Locate every Plasmodium ovale-infected red blood cell.
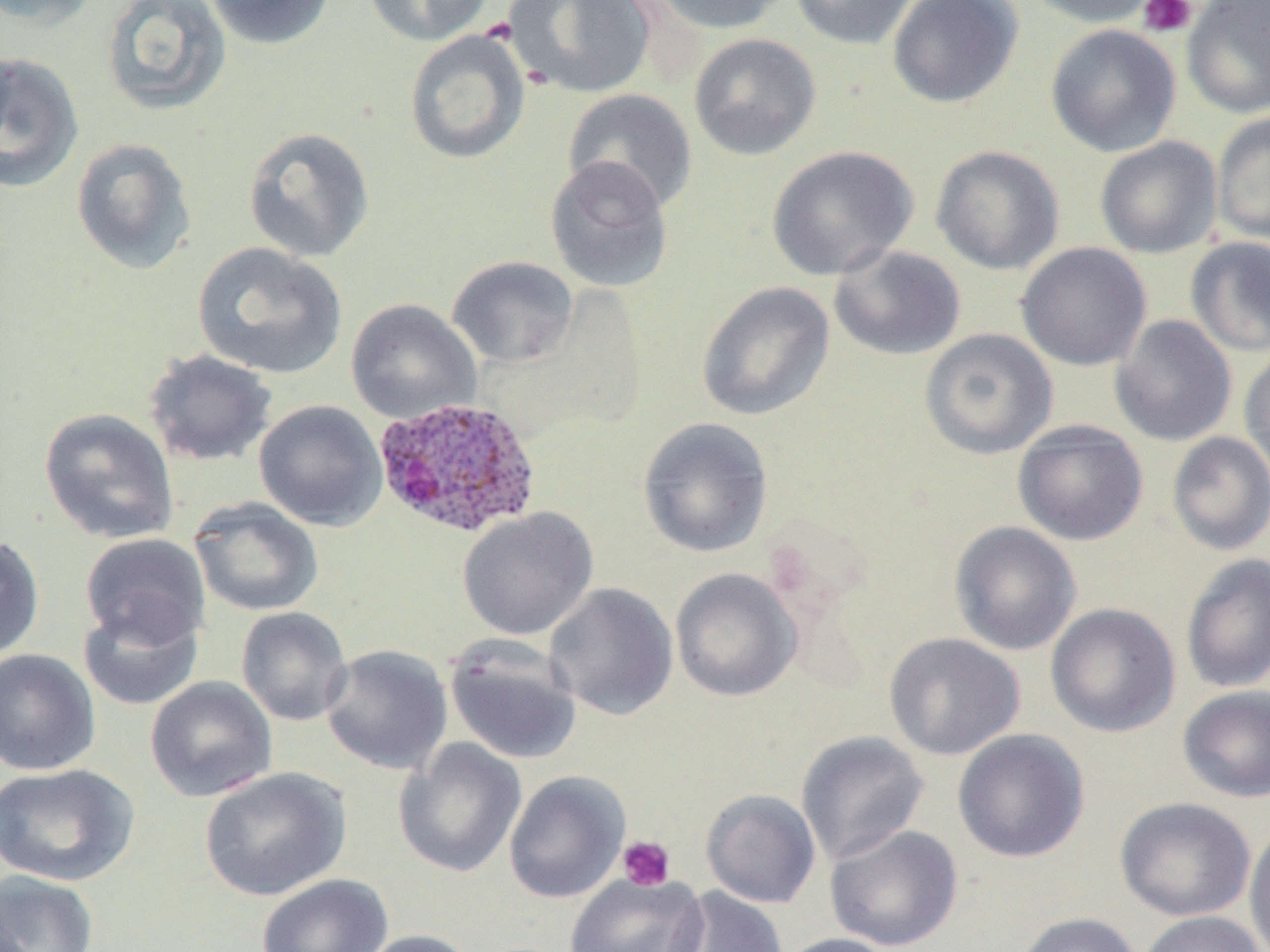

Approximate bounding boxes as (x1,y1)-(x2,y2) corner pairs in pixels.
Plasmodium ovale-infected red blood cells: (372,396)-(542,540).

{
  "slide_level_diagnosis": "Plasmodium ovale",
  "magnification": "1000x",
  "image_size": "1270×952 pixels",
  "stain": "May-Grünwald-Giemsa",
  "platelet_locations": "approximate bounding boxes as (x1,y1)-(x2,y2) corner pairs in pixels: (1137,0)-(1198,38), (617,835)-(675,891)",
  "preparation": "thin blood smear",
  "modality": "optical microscopy",
  "field_of_view": "single",
  "uninfected_red_blood_cell_locations": "approximate bounding boxes as (x1,y1)-(x2,y2) corner pairs in pixels: (1,0)-(102,31), (204,0)-(336,50), (363,0)-(493,46), (503,0)-(657,100), (641,0)-(790,35), (789,0)-(920,49), (888,0)-(1024,108), (1023,0)-(1163,28), (1181,0)-(1270,119), (99,1)-(232,116), (1045,23)-(1181,157), (404,29)-(531,165), (689,33)-(821,161), (0,46)-(17,152), (0,51)-(84,193), (562,89)-(697,213), (1211,111)-(1270,245), (242,126)-(376,263), (1094,136)-(1223,259), (71,137)-(197,276), (766,145)-(919,281), (930,145)-(1065,275), (544,155)-(674,293), (1185,237)-(1270,356), (191,242)-(348,380), (1016,242)-(1151,371), (829,245)-(966,361), (446,255)-(579,367), (695,281)-(835,422), (345,298)-(482,423), (1109,314)-(1237,447), (919,328)-(1058,460), (1239,346)-(1270,483), (143,349)-(278,467), (253,399)-(388,531), (38,407)-(180,545), (637,417)-(774,558), (1012,420)-(1148,546), (1166,431)-(1270,555), (189,497)-(324,617), (457,507)-(598,640), (949,521)-(1081,656), (79,532)-(211,650), (0,534)-(45,662), (1180,553)-(1270,693), (670,568)-(802,702), (543,582)-(679,721), (78,600)-(204,712), (1046,602)-(1180,737), (235,607)-(353,727), (883,632)-(1025,760), (444,634)-(583,765), (320,644)-(453,776), (0,648)-(101,776), (144,676)-(278,803), (1178,685)-(1270,802), (952,728)-(1089,863), (795,730)-(930,865), (393,737)-(527,878), (1,763)-(141,887), (199,767)-(350,901), (504,770)-(631,904), (700,788)-(821,908), (1115,796)-(1256,922), (1244,822)-(1270,952), (824,824)-(963,952), (1,870)-(98,952), (256,873)-(394,952), (565,873)-(710,952), (668,887)-(789,952), (1136,911)-(1265,952), (1014,912)-(1142,952), (352,929)-(479,952), (776,933)-(901,952)"
}